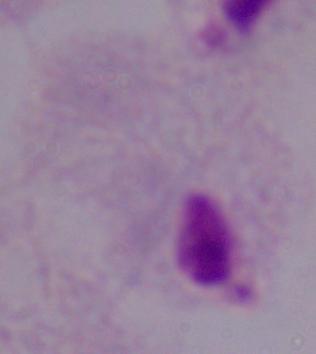

{
  "magnification": "1000x",
  "identification": "trichomonad",
  "modality": "micrograph"
}